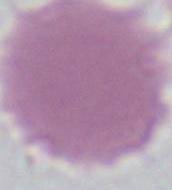
Photomicrograph. A red blood cell is seen. Captured at 1000x magnification.